Assess for malaria.
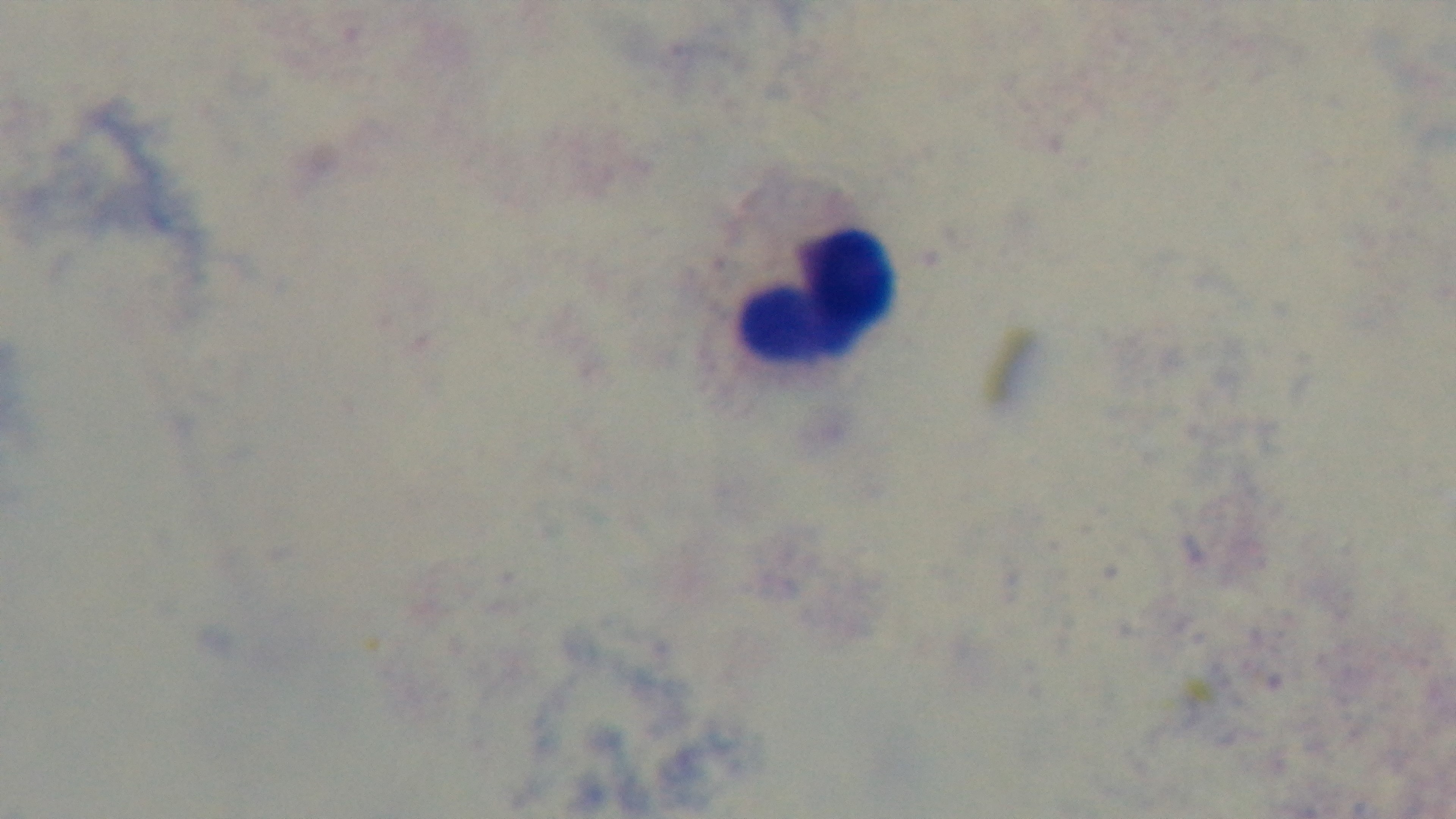

Negative.

Summary:
  - Capture: mounted 4K digital camera
  - Preparation: thick smear
  - Field of view: one from the slide
  - Objective: 100x oil immersion
  - Stain: Giemsa
  - Modality: light microscopy